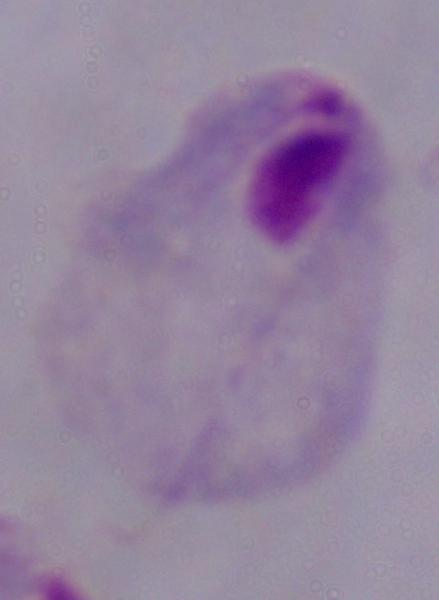
Captured at 1000x magnification. A trichomonad is seen. Micrograph.